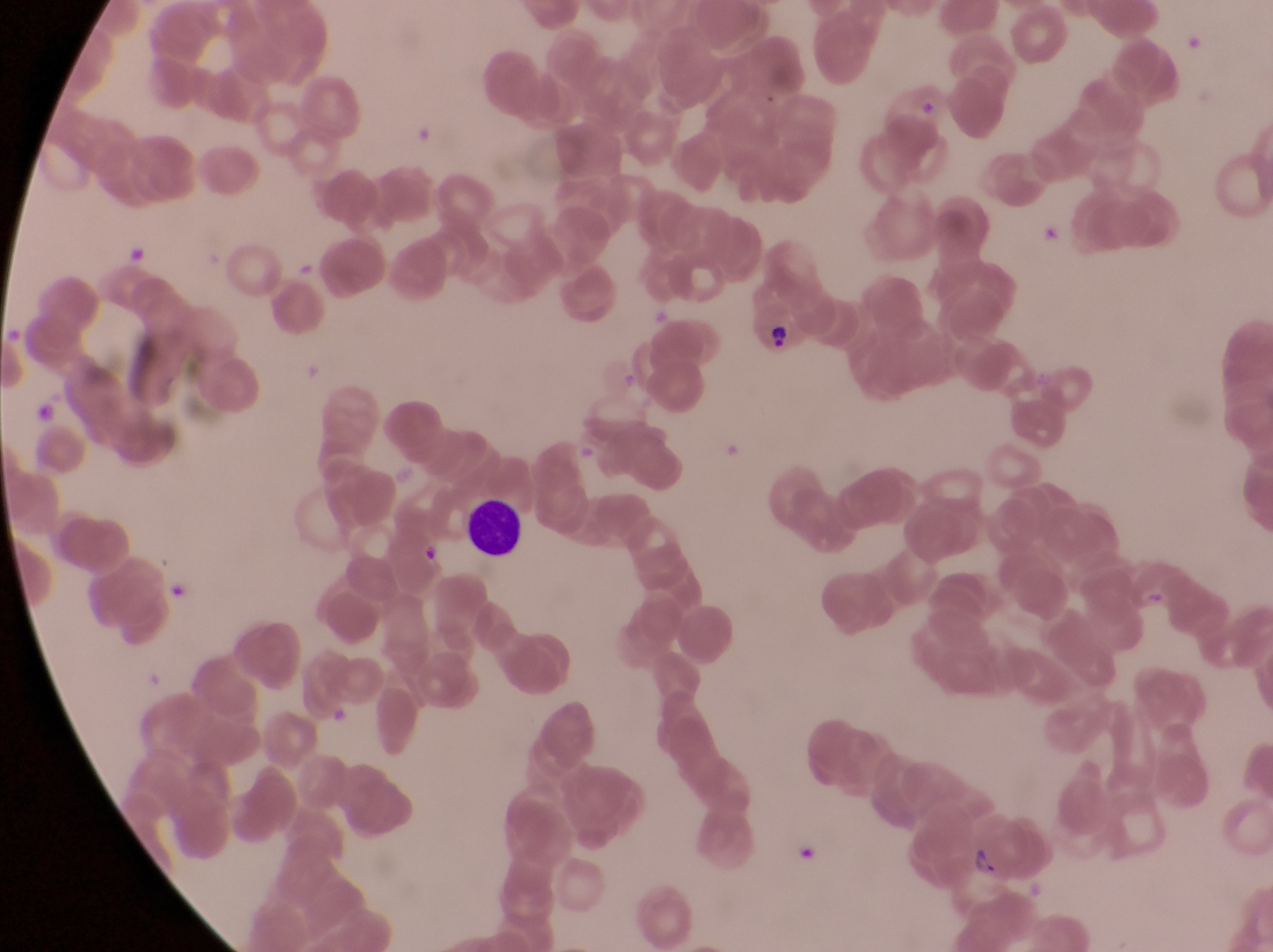

Approximate bounding boxes as [left, top, right, bottom] in pixels. Parasitised red blood cell locations: [741, 289, 813, 359], [968, 826, 1038, 888]. Leukocyte locations: [468, 505, 523, 560], [170, 579, 194, 605]. Artifact (platelet-like body, stain precipitate, or debris) locations: [127, 240, 151, 266], [650, 305, 670, 326], [33, 401, 59, 421]. Thin blood film. Single field of view. Sample from Uganda. At a magnification of 1000x. Image is 1273×952 pixels. Captured by a smartphone held over the eyepiece of an Olympus CX-23 microscope.